Give the extent of all Plasmodium malariae-infected red blood cells.
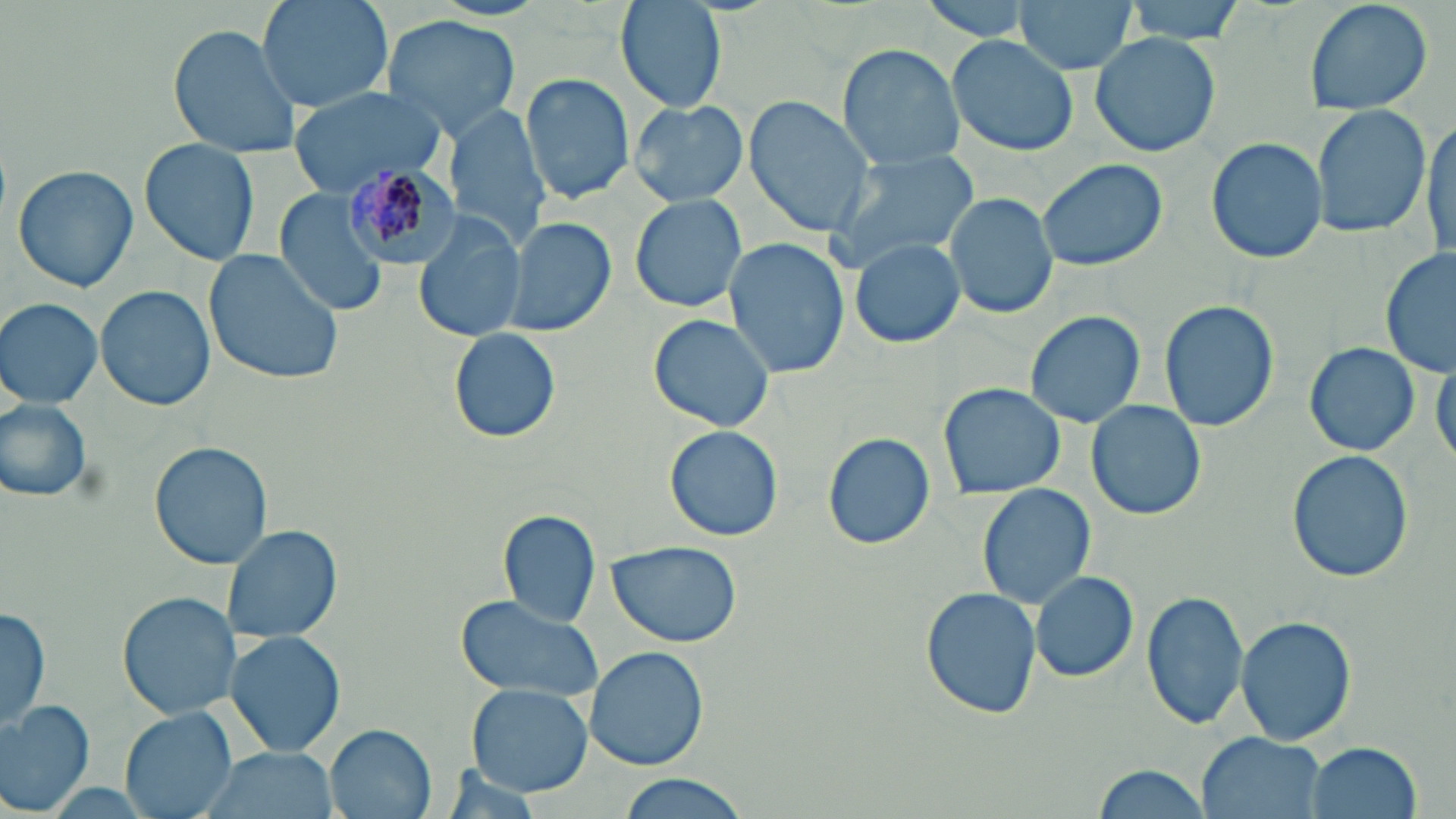
Approximate bounding boxes as (x1,y1)-(x2,y2) corner pairs in pixels.
Plasmodium malariae-infected red blood cells: (342,161)-(465,274).

slide-level diagnosis = Plasmodium malariae
image size = 1456×819 pixels
field of view = one of a larger specimen
modality = light microscopy
preparation = thin blood film
stain = May-Grünwald-Giemsa
uninfected red blood cell locations = approximate bounding boxes as (x1,y1)-(x2,y2) corner pairs in pixels: (257,0)-(392,115), (917,0)-(1042,40), (1015,0)-(1136,75), (1118,0)-(1249,42), (1302,0)-(1436,116), (615,1)-(726,113), (379,14)-(522,138), (166,23)-(303,160), (1089,30)-(1221,158), (948,34)-(1077,156), (835,43)-(966,170), (520,72)-(635,206), (288,87)-(445,196), (744,95)-(875,237), (626,99)-(750,206), (1312,106)-(1431,238), (444,107)-(551,249), (1420,115)-(1453,265), (1205,135)-(1326,264), (138,140)-(259,267), (823,148)-(981,274), (1037,159)-(1168,272), (12,165)-(139,291), (276,192)-(394,319), (946,192)-(1059,321), (630,193)-(747,314), (412,212)-(524,342), (500,216)-(617,337), (848,237)-(963,348), (722,239)-(850,380), (204,248)-(345,386), (1379,248)-(1455,379), (95,285)-(214,409), (0,297)-(102,409), (1159,299)-(1279,433), (1023,309)-(1145,429), (648,313)-(774,433), (447,326)-(562,444), (1302,341)-(1421,458), (1431,350)-(1456,473), (1298,361)-(1419,556), (938,383)-(1066,498), (0,398)-(98,506), (1087,399)-(1206,521), (665,425)-(784,541), (822,431)-(936,551), (149,441)-(271,571), (1286,451)-(1414,584), (977,483)-(1096,611), (500,509)-(602,626), (224,523)-(342,645), (607,540)-(741,648), (1028,570)-(1138,684), (920,587)-(1042,721), (1141,590)-(1249,729), (117,591)-(240,720), (453,592)-(606,704), (1,605)-(52,730), (1234,614)-(1358,749), (226,628)-(345,756), (585,646)-(707,771), (467,685)-(593,796), (0,699)-(97,815), (121,708)-(236,819), (326,725)-(437,819), (1197,731)-(1326,819), (1305,740)-(1422,818), (195,746)-(342,819), (1090,763)-(1210,819), (615,774)-(753,818)
magnification = 1000x